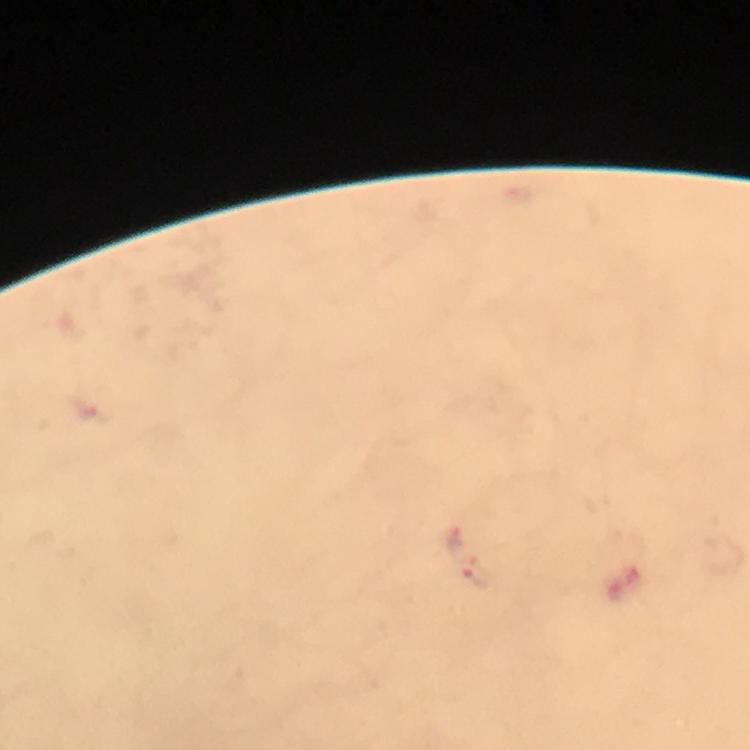 Approximate centers as [x, y] in pixels. Plasmodium parasite locations: [454, 538], [477, 577]. Immersion oil applied. A crop from one field of view. Giemsa stain. Image is 750×750 pixels. Thick blood smear. Photographed through the microscope with a smartphone camera. 100x magnification. From a diagnostic examination for malaria.